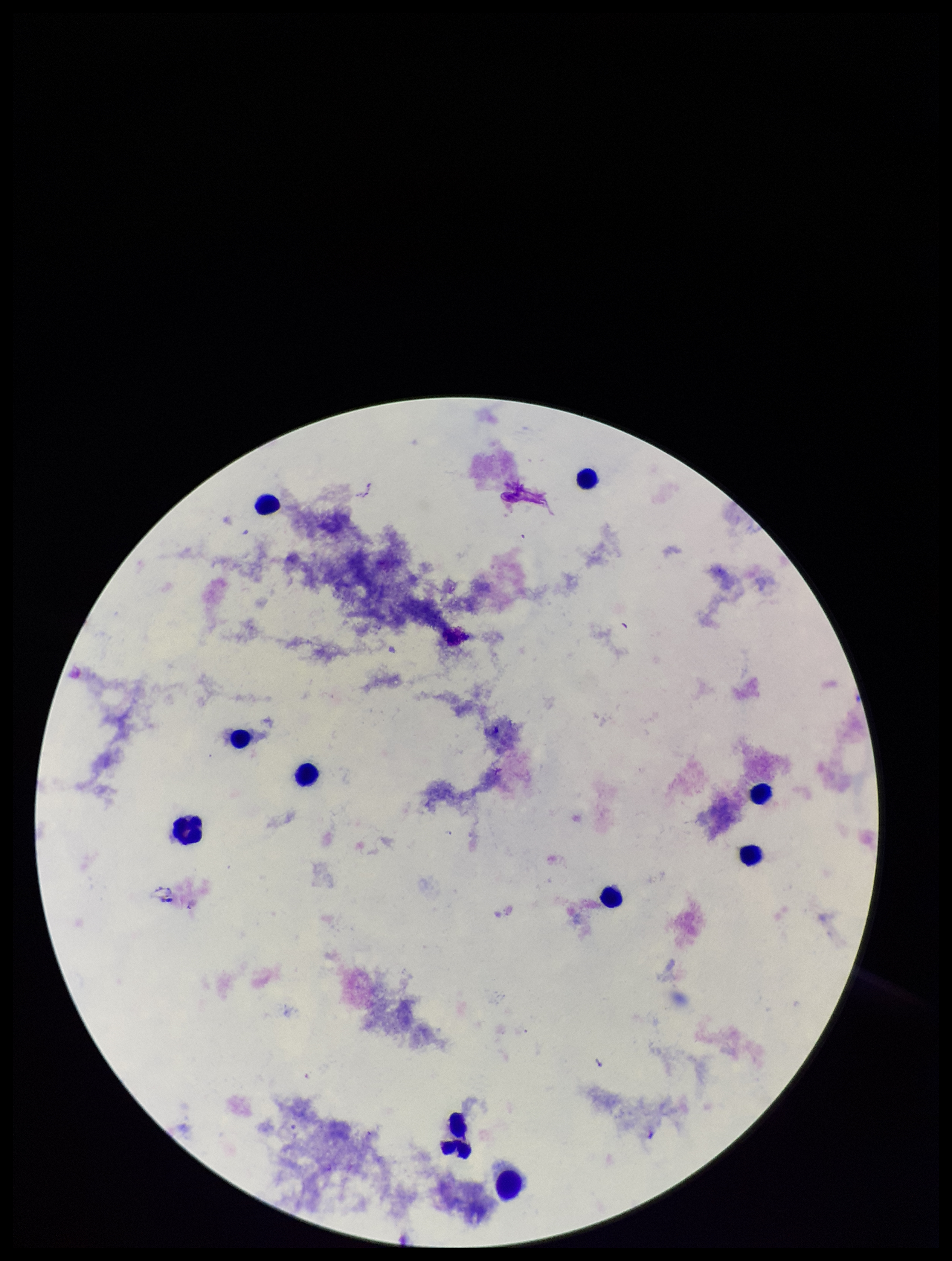

Summary:
  - Leukocyte count: 10
  - Capture: smartphone photograph through the microscope eyepiece
  - Patient malaria status: negative
  - Preparation: thick
  - Stain: Giemsa
  - Plasmodium parasites: none detected
  - Image size: 952×1261 pixels
  - Parasite count: 0
  - Field of view: single